State the blood parasite species.
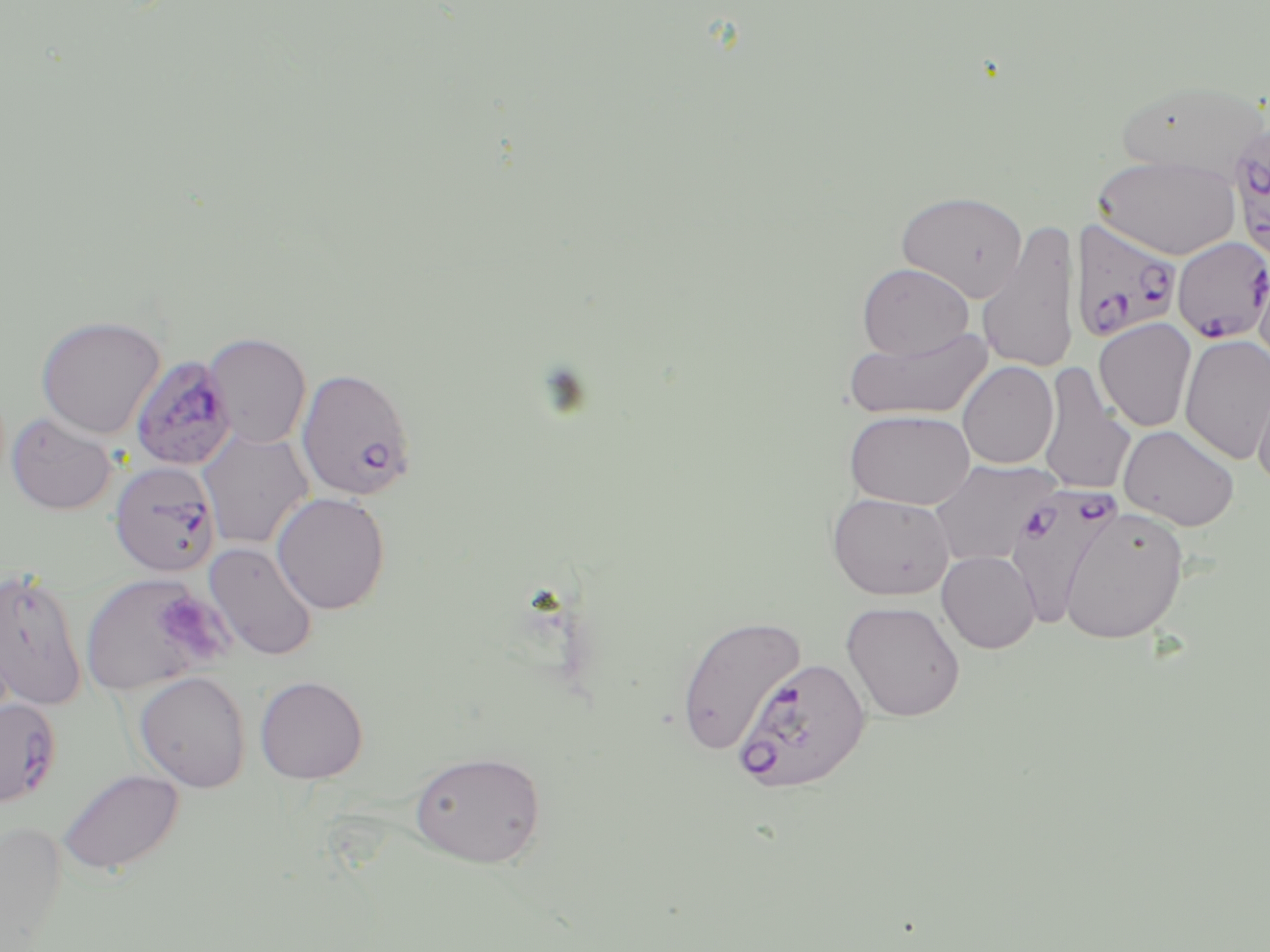
Plasmodium falciparum.

{
  "preparation": "thin blood smear",
  "stain": "May-Grünwald-Giemsa",
  "modality": "optical microscopy",
  "plasmodium_falciparum_infected_red_blood_cell_locations": "approximate bounding boxes as (x1,y1)-(x2,y2) corner pairs in pixels: (1226,119)-(1270,267), (1069,217)-(1183,343), (1172,236)-(1270,343), (130,355)-(236,471), (296,367)-(416,500), (109,461)-(221,577), (1003,486)-(1124,630), (0,566)-(88,710), (732,657)-(871,795), (0,697)-(61,807)",
  "magnification": "1000x",
  "field_of_view": "single",
  "image_size": "1270×952 pixels",
  "platelet_locations": "approximate bounding boxes as (x1,y1)-(x2,y2) corner pairs in pixels: (168,594)-(219,658)",
  "uninfected_red_blood_cell_locations": "approximate bounding boxes as (x1,y1)-(x2,y2) corner pairs in pixels: (1115,77)-(1268,182), (1093,154)-(1240,260), (896,190)-(1028,302), (977,219)-(1082,374), (1253,254)-(1270,373), (857,263)-(973,360), (35,315)-(166,439), (1094,318)-(1197,432), (843,326)-(994,421), (204,332)-(312,448), (1179,334)-(1270,464), (958,361)-(1058,469), (1037,363)-(1136,495), (1251,367)-(1270,492), (844,410)-(975,510), (7,412)-(117,515), (1118,425)-(1240,531), (198,430)-(314,550), (928,458)-(1060,567), (827,491)-(955,600), (271,492)-(391,614), (1058,505)-(1189,644), (205,542)-(318,661), (937,550)-(1041,653), (79,573)-(219,695), (841,601)-(965,722), (675,614)-(805,755), (134,671)-(251,792), (254,675)-(368,784), (410,750)-(546,868), (57,768)-(185,877), (0,821)-(68,950)"
}